Identify the parasite.
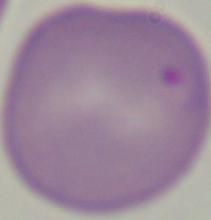

Babesia.

Captured at 1000x magnification. Micrograph.